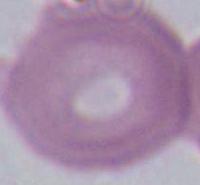

Captured at 1000x magnification. An erythrocyte is shown. Photomicrograph.